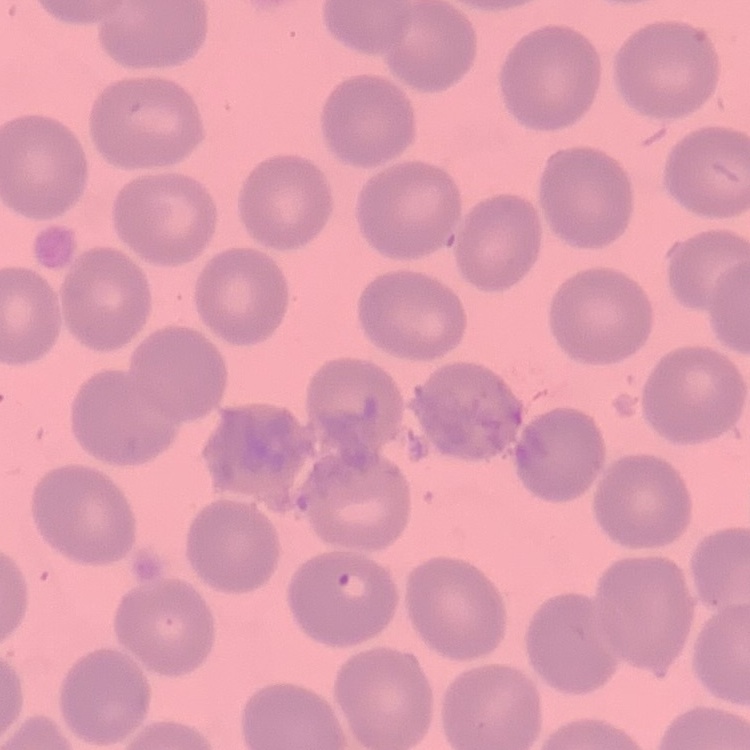
Summary:
  - Red blood cell morphology: no rouleaux formation
  - Image type: one tile cut from a larger photomicrograph
  - Preparation: thin peripheral smear
  - Stain: Field's or Giemsa